Report the malaria status of this cell.
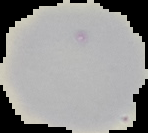
It is uninfected.

Summary:
  - Image type: segmented cell region with the area outside set to black
  - Image size: 148×133 pixels
  - Preparation: thin blood smear